Describe the morphology of the red blood cells.
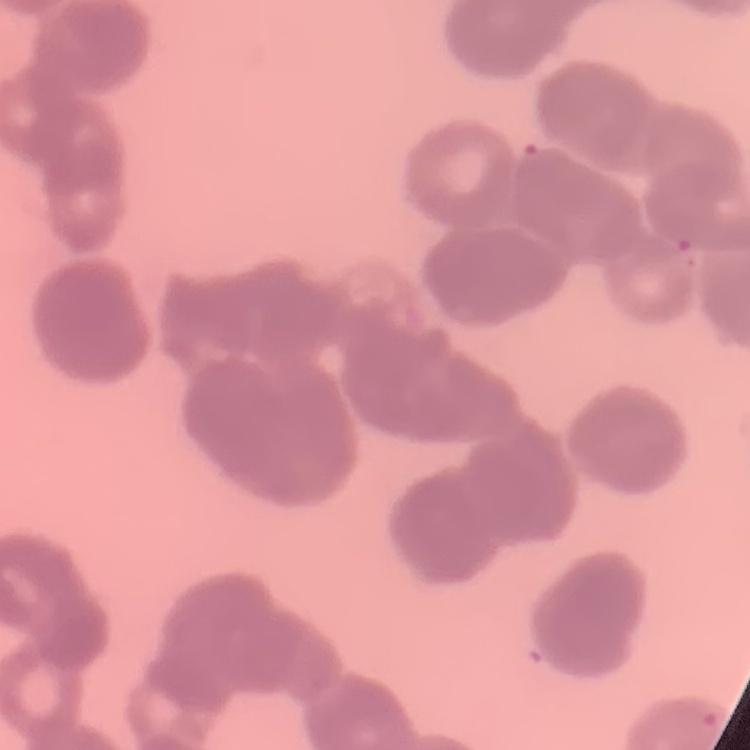
Rouleaux formation.

One tile cut from a larger photomicrograph. Stained with either Field's or Giemsa. Thin blood film.